Locate and identify every blood parasite.
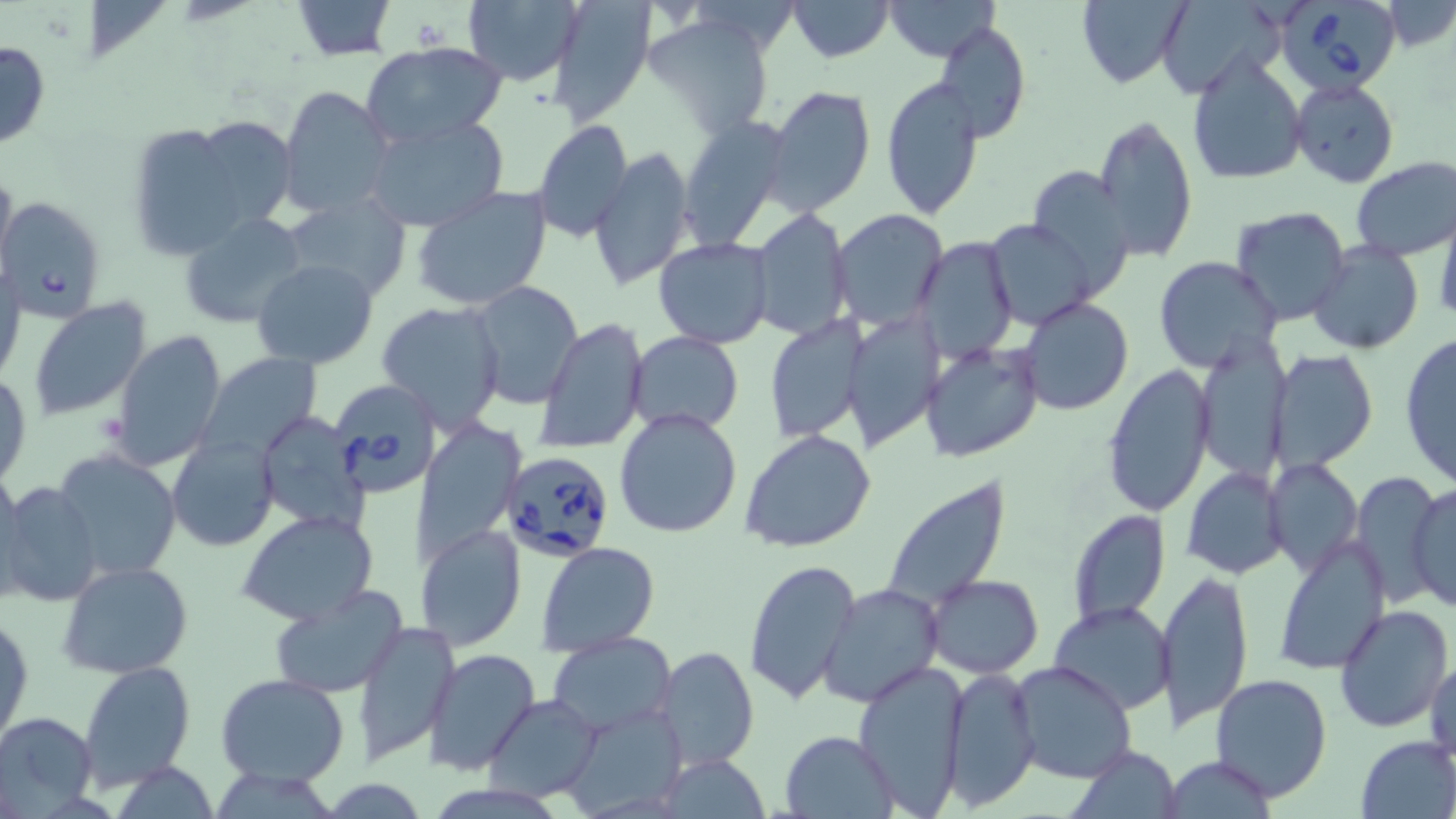

Approximate bounding boxes as (x1, y1, x2, y2) in pixels.
Babesia divergens-infected red blood cells: (1282, 2, 1406, 106), (0, 196, 107, 321), (326, 380, 443, 500), (498, 452, 615, 562).
No Plasmodium falciparum, Plasmodium ovale, Plasmodium malariae, Plasmodium vivax, or Trypanosoma brucei observed.

Summary:
  - Uninfected red blood cell locations: (290, 0, 395, 59), (788, 0, 893, 61), (882, 0, 1000, 62), (1078, 0, 1194, 89), (547, 1, 655, 125), (1156, 1, 1285, 99), (463, 2, 583, 85), (1383, 2, 1456, 50), (644, 14, 775, 138), (936, 18, 1032, 144), (0, 38, 50, 151), (360, 41, 509, 149), (1187, 51, 1308, 186), (881, 74, 985, 220), (1290, 78, 1399, 189), (763, 85, 876, 217), (277, 86, 396, 218), (364, 114, 509, 232), (1093, 114, 1198, 261), (188, 115, 297, 232), (679, 117, 792, 249), (533, 119, 633, 241), (126, 122, 259, 259), (591, 145, 697, 294), (1351, 156, 1456, 261), (0, 160, 16, 276), (1026, 167, 1135, 294), (411, 186, 554, 311), (281, 188, 410, 300), (1231, 206, 1352, 325), (752, 208, 851, 340), (830, 209, 947, 329), (178, 212, 310, 329), (1432, 213, 1454, 327), (985, 219, 1096, 330), (653, 237, 776, 349), (914, 237, 1018, 361), (1307, 239, 1425, 354), (1153, 255, 1281, 374), (251, 257, 380, 368), (0, 262, 25, 387), (468, 282, 585, 410), (1019, 297, 1134, 416), (27, 298, 154, 423), (376, 301, 507, 431), (846, 316, 941, 450), (535, 317, 649, 455), (762, 319, 868, 444), (110, 329, 228, 470), (628, 331, 744, 433), (1398, 333, 1456, 488), (1194, 334, 1292, 483), (920, 340, 1043, 463), (1267, 349, 1377, 471), (196, 350, 322, 464), (1101, 363, 1216, 516), (0, 372, 32, 490), (614, 406, 744, 539), (256, 411, 370, 533), (195, 419, 349, 552), (414, 421, 524, 568), (739, 428, 877, 553), (169, 435, 277, 552), (52, 449, 182, 581), (1265, 457, 1362, 577), (0, 466, 25, 600), (1182, 467, 1290, 579), (1349, 470, 1443, 608), (0, 479, 103, 606), (884, 479, 1010, 611), (1408, 479, 1455, 614), (1067, 509, 1170, 629), (237, 510, 379, 626), (416, 523, 527, 651), (1274, 536, 1391, 677), (536, 540, 659, 656), (743, 558, 861, 708), (58, 562, 192, 678), (1162, 569, 1253, 731), (925, 574, 1043, 677), (819, 581, 944, 706), (268, 584, 410, 700), (1048, 601, 1174, 715), (1334, 605, 1454, 733), (1, 610, 33, 748), (352, 619, 460, 764), (547, 632, 677, 736), (654, 646, 760, 772), (425, 649, 540, 773), (1427, 655, 1456, 766), (77, 661, 196, 787), (1009, 661, 1137, 784), (855, 665, 970, 815), (943, 666, 1040, 811), (1208, 671, 1333, 801), (216, 672, 349, 787), (482, 693, 602, 802), (0, 710, 99, 814), (782, 730, 898, 816), (1355, 735, 1456, 817), (1069, 745, 1179, 819), (656, 752, 771, 817), (1166, 754, 1280, 818)
  - Slide-level diagnosis: Babesia divergens
  - Magnification: 1000x
  - Stain: May-Grünwald-Giemsa
  - Modality: optical microscopy
  - Image size: 1456×819 pixels
  - Field of view: single
  - Preparation: thin blood film